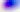
{
  "magnification": "400x",
  "identification": "Toxoplasma gondii",
  "modality": "micrograph"
}